Classify the preparation.
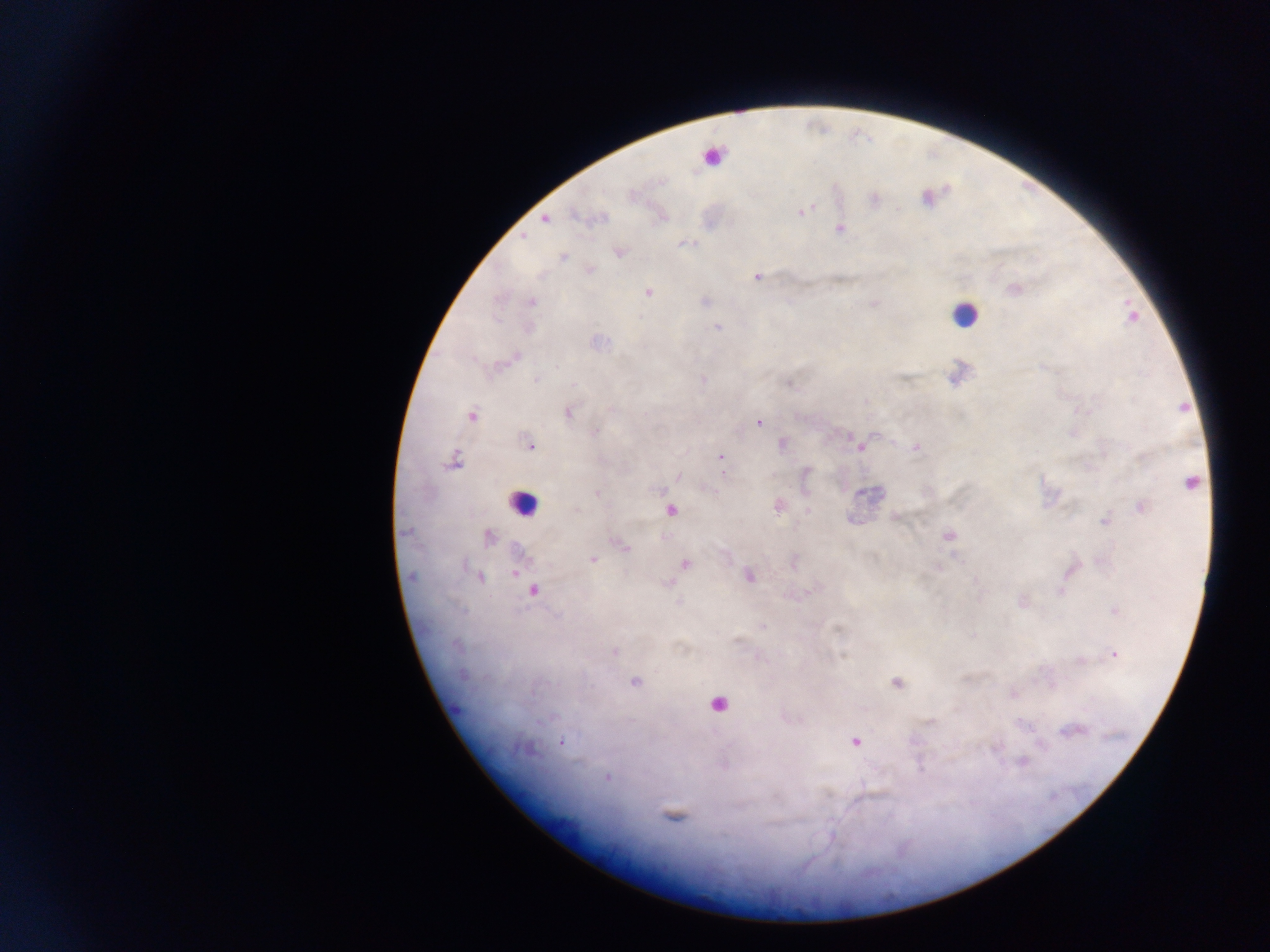
Thick blood film.

Approximate centers as {x, y} in pixels. Malaria parasite locations: {803, 211}, {544, 219}, {839, 229}, {523, 237}, {620, 252}, {563, 257}, {591, 270}, {757, 277}, {1014, 290}, {648, 293}, {531, 302}, {717, 326}, {515, 358}, {536, 379}, {703, 380}, {568, 412}, {1086, 412}, {471, 416}, {759, 422}, {595, 431}, {853, 439}, {782, 444}, {529, 445}, {859, 446}, {916, 447}, {720, 457}, {454, 462}, {679, 476}, {1192, 483}, {661, 491}, {597, 494}, {777, 505}, {1141, 507}, {577, 509}, {808, 511}, {1104, 521}, {405, 531}, {948, 535}, {490, 537}, {621, 545}, {593, 560}, {686, 564}, {515, 570}, {749, 576}, {480, 577}, {411, 578}, {533, 591}, {1061, 591}, {808, 592}, {678, 601}, {1115, 611}, {763, 627}, {456, 646}, {615, 652}, {1115, 654}, {635, 682}, {896, 683}, {540, 721}, {930, 722}, {1023, 724}, {1073, 730}, {855, 741}, {562, 742}, {1041, 745}, {524, 750}, {1022, 762}, {606, 778}. Leukocyte locations: {717, 157}, {964, 314}, {522, 504}, {671, 510}, {718, 704}. Collected in Ghana. Photographed through a microscope with a mobile-phone camera. Single field of view. Image is 1270×952 pixels.